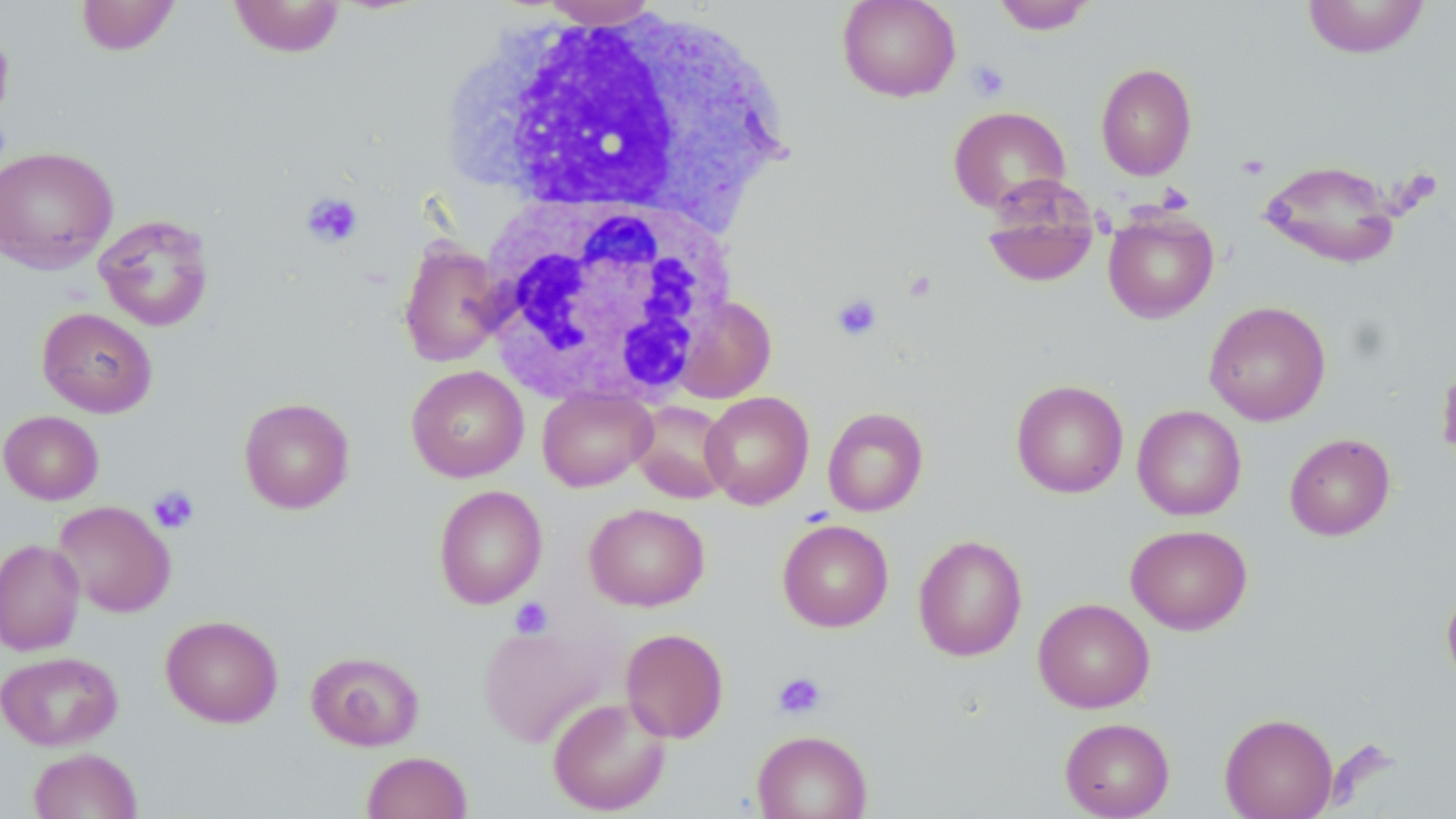
Summary:
  - Coordinate format: approximate bounding boxes as (x1,y1)-(x2,y2) corner pairs in pixels
  - White blood cell locations: (466,8)-(783,226), (480,196)-(732,408)
  - Platelet locations: (966,60)-(1010,102), (1236,153)-(1270,180), (301,192)-(364,248), (830,292)-(883,342), (148,486)-(200,534), (510,597)-(553,638), (773,672)-(827,719)
  - Uninfected red blood cell locations: (75,0)-(181,56), (228,0)-(347,58), (538,0)-(661,29), (837,0)-(961,102), (992,0)-(1097,34), (1301,0)-(1431,59), (1096,62)-(1197,180), (947,105)-(1071,215), (0,146)-(118,274), (1259,160)-(1402,269), (980,180)-(1100,290), (1103,209)-(1219,323), (94,213)-(215,331), (398,237)-(508,368), (673,296)-(776,404), (1204,301)-(1331,425), (37,307)-(158,417), (1436,355)-(1456,467), (406,365)-(529,482), (1011,379)-(1128,498), (537,388)-(656,491), (1010,390)-(1248,503), (700,391)-(814,509), (238,396)-(355,514), (630,399)-(733,503), (1132,405)-(1246,520), (822,407)-(929,516), (1,411)-(104,505), (1284,433)-(1395,541), (433,485)-(547,608), (53,500)-(176,617), (584,503)-(709,611), (777,519)-(894,632), (1126,524)-(1253,635), (913,535)-(1028,662), (0,538)-(85,655), (1442,584)-(1456,690), (1033,597)-(1155,713), (161,615)-(283,728), (477,621)-(615,747), (620,628)-(729,743), (306,649)-(425,751), (0,650)-(123,751), (548,695)-(671,816), (1219,712)-(1339,819), (1060,717)-(1175,819), (752,730)-(872,819), (28,748)-(142,819), (362,751)-(472,819)
  - Slide-level diagnosis: no evidence of blood parasites
  - Preparation: thin blood film
  - Magnification: 1000x
  - Field of view: one of a larger specimen
  - Stain: May-Grünwald-Giemsa
  - Image size: 1456×819 pixels
  - Modality: light microscopy